Identify the blood parasite species.
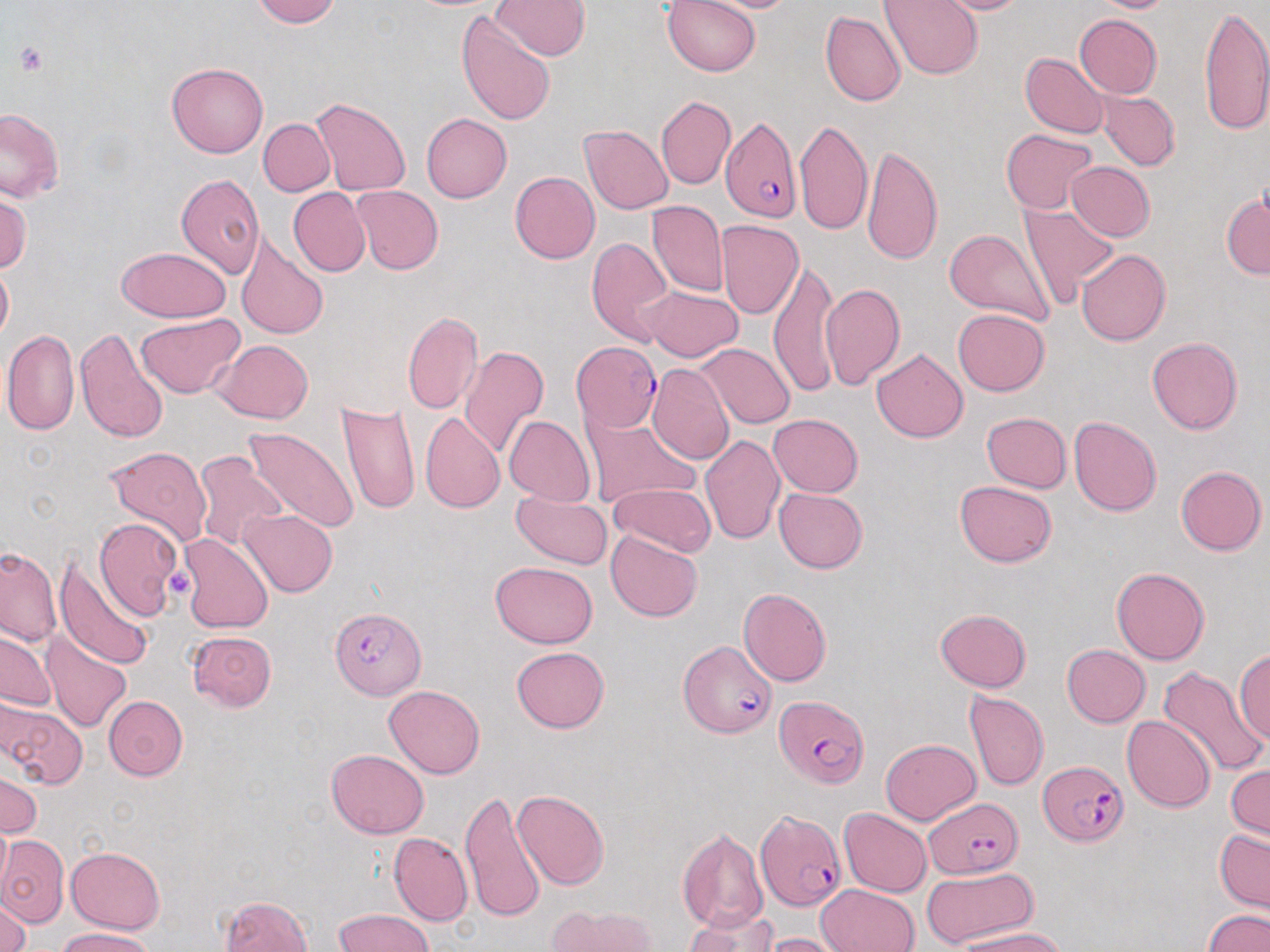
Plasmodium falciparum.

Approximate bounding boxes as named x1/y1/x2/y2 corners in pixels. Uninfected red blood cell locations: (x1=251, y1=0, x2=339, y2=26), (x1=493, y1=0, x2=591, y2=60), (x1=662, y1=0, x2=761, y2=77), (x1=691, y1=0, x2=805, y2=13), (x1=877, y1=0, x2=983, y2=80), (x1=922, y1=0, x2=1035, y2=15), (x1=1086, y1=0, x2=1179, y2=13), (x1=1198, y1=3, x2=1270, y2=136), (x1=820, y1=10, x2=906, y2=107), (x1=456, y1=11, x2=555, y2=126), (x1=1074, y1=13, x2=1162, y2=98), (x1=1019, y1=52, x2=1110, y2=138), (x1=167, y1=61, x2=268, y2=158), (x1=1096, y1=90, x2=1179, y2=171), (x1=656, y1=96, x2=735, y2=190), (x1=309, y1=97, x2=411, y2=196), (x1=0, y1=108, x2=65, y2=203), (x1=421, y1=112, x2=511, y2=202), (x1=259, y1=118, x2=335, y2=196), (x1=796, y1=119, x2=872, y2=238), (x1=815, y1=121, x2=917, y2=247), (x1=579, y1=124, x2=674, y2=215), (x1=1001, y1=128, x2=1098, y2=213), (x1=860, y1=144, x2=944, y2=265), (x1=1066, y1=162, x2=1155, y2=241), (x1=510, y1=171, x2=601, y2=264), (x1=176, y1=173, x2=265, y2=278), (x1=352, y1=185, x2=443, y2=274), (x1=288, y1=188, x2=370, y2=277), (x1=1221, y1=190, x2=1270, y2=279), (x1=0, y1=191, x2=31, y2=275), (x1=648, y1=201, x2=728, y2=297), (x1=1018, y1=202, x2=1121, y2=306), (x1=716, y1=219, x2=804, y2=319), (x1=945, y1=228, x2=1056, y2=327), (x1=236, y1=236, x2=329, y2=339), (x1=587, y1=236, x2=673, y2=345), (x1=116, y1=246, x2=231, y2=323), (x1=1076, y1=248, x2=1170, y2=346), (x1=769, y1=258, x2=840, y2=396), (x1=0, y1=259, x2=12, y2=345), (x1=820, y1=284, x2=905, y2=389), (x1=640, y1=285, x2=745, y2=362), (x1=953, y1=308, x2=1049, y2=396), (x1=402, y1=312, x2=482, y2=415), (x1=136, y1=313, x2=245, y2=399), (x1=76, y1=328, x2=168, y2=444), (x1=3, y1=330, x2=79, y2=436), (x1=1146, y1=337, x2=1244, y2=434), (x1=215, y1=339, x2=313, y2=423), (x1=697, y1=343, x2=795, y2=429), (x1=459, y1=346, x2=549, y2=459), (x1=872, y1=347, x2=968, y2=443), (x1=646, y1=364, x2=735, y2=466), (x1=337, y1=401, x2=421, y2=515), (x1=981, y1=411, x2=1072, y2=492), (x1=420, y1=412, x2=505, y2=513), (x1=582, y1=414, x2=699, y2=509), (x1=769, y1=414, x2=862, y2=496), (x1=969, y1=414, x2=1068, y2=565), (x1=504, y1=415, x2=594, y2=506), (x1=1070, y1=415, x2=1163, y2=516), (x1=243, y1=425, x2=360, y2=533), (x1=700, y1=434, x2=784, y2=545), (x1=105, y1=445, x2=212, y2=549), (x1=193, y1=452, x2=288, y2=552), (x1=1176, y1=465, x2=1267, y2=556), (x1=954, y1=481, x2=1056, y2=567), (x1=608, y1=483, x2=715, y2=557), (x1=775, y1=488, x2=868, y2=574), (x1=512, y1=490, x2=612, y2=570), (x1=240, y1=508, x2=337, y2=596), (x1=94, y1=516, x2=182, y2=620), (x1=606, y1=531, x2=702, y2=622), (x1=180, y1=533, x2=272, y2=633), (x1=0, y1=546, x2=61, y2=645), (x1=53, y1=554, x2=154, y2=668), (x1=490, y1=560, x2=598, y2=648), (x1=503, y1=562, x2=604, y2=732), (x1=1111, y1=566, x2=1210, y2=665), (x1=738, y1=588, x2=832, y2=687), (x1=935, y1=608, x2=1031, y2=692), (x1=42, y1=631, x2=130, y2=731), (x1=187, y1=631, x2=277, y2=711), (x1=0, y1=632, x2=58, y2=712), (x1=1062, y1=644, x2=1151, y2=727), (x1=510, y1=647, x2=610, y2=733), (x1=1235, y1=649, x2=1270, y2=748), (x1=1160, y1=666, x2=1269, y2=777), (x1=383, y1=685, x2=486, y2=778), (x1=964, y1=690, x2=1049, y2=792), (x1=104, y1=695, x2=188, y2=780), (x1=2, y1=701, x2=87, y2=788), (x1=1122, y1=715, x2=1217, y2=813), (x1=881, y1=739, x2=980, y2=824), (x1=325, y1=749, x2=429, y2=838), (x1=1228, y1=763, x2=1270, y2=842), (x1=0, y1=770, x2=40, y2=838), (x1=461, y1=789, x2=546, y2=924), (x1=512, y1=789, x2=609, y2=890), (x1=838, y1=808, x2=931, y2=897), (x1=0, y1=821, x2=11, y2=897), (x1=677, y1=827, x2=769, y2=933), (x1=1215, y1=829, x2=1270, y2=913), (x1=389, y1=832, x2=473, y2=926), (x1=1, y1=837, x2=68, y2=927), (x1=68, y1=846, x2=164, y2=933), (x1=921, y1=866, x2=1037, y2=950), (x1=817, y1=884, x2=918, y2=952), (x1=0, y1=893, x2=32, y2=952), (x1=220, y1=894, x2=313, y2=952), (x1=546, y1=904, x2=658, y2=952), (x1=335, y1=909, x2=433, y2=952), (x1=687, y1=909, x2=780, y2=952), (x1=1205, y1=910, x2=1269, y2=952), (x1=55, y1=927, x2=157, y2=952), (x1=956, y1=928, x2=1065, y2=952), (x1=761, y1=932, x2=845, y2=952). Plasmodium falciparum-infected red blood cell locations: (x1=721, y1=113, x2=802, y2=223), (x1=571, y1=341, x2=661, y2=432), (x1=328, y1=605, x2=426, y2=700), (x1=678, y1=638, x2=776, y2=737), (x1=775, y1=695, x2=868, y2=787), (x1=1040, y1=762, x2=1127, y2=844), (x1=924, y1=797, x2=1024, y2=878), (x1=756, y1=811, x2=845, y2=911). Platelet locations: (x1=13, y1=42, x2=49, y2=76), (x1=164, y1=567, x2=195, y2=600). May-Grünwald-Giemsa-stained preparation. One field of a larger specimen. 1000x magnification. Light microscopy. Thin blood smear. Image is 1270×952 pixels.